Assess this cell for malaria.
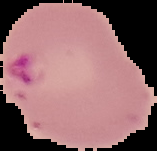

It is parasitized.

image type = cell region segmented out of the field of view; surrounding area masked to black
preparation = thin blood film
image size = 157×151 pixels